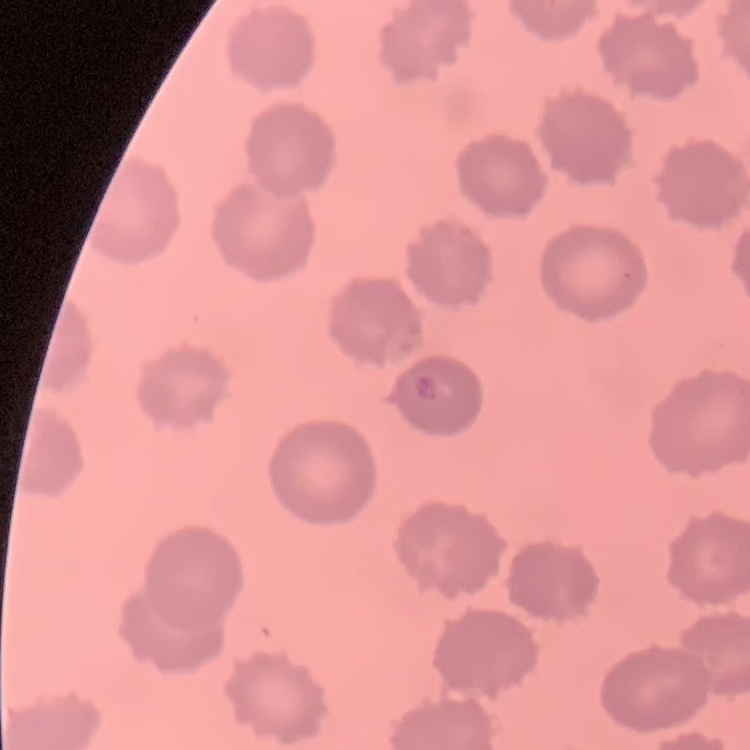
erythrocyte_morphology: no rouleaux formation
stain: Field's or Giemsa
image_type: square crop of a larger photomicrograph
preparation: thin blood smear